Find each parasitized red blood cell.
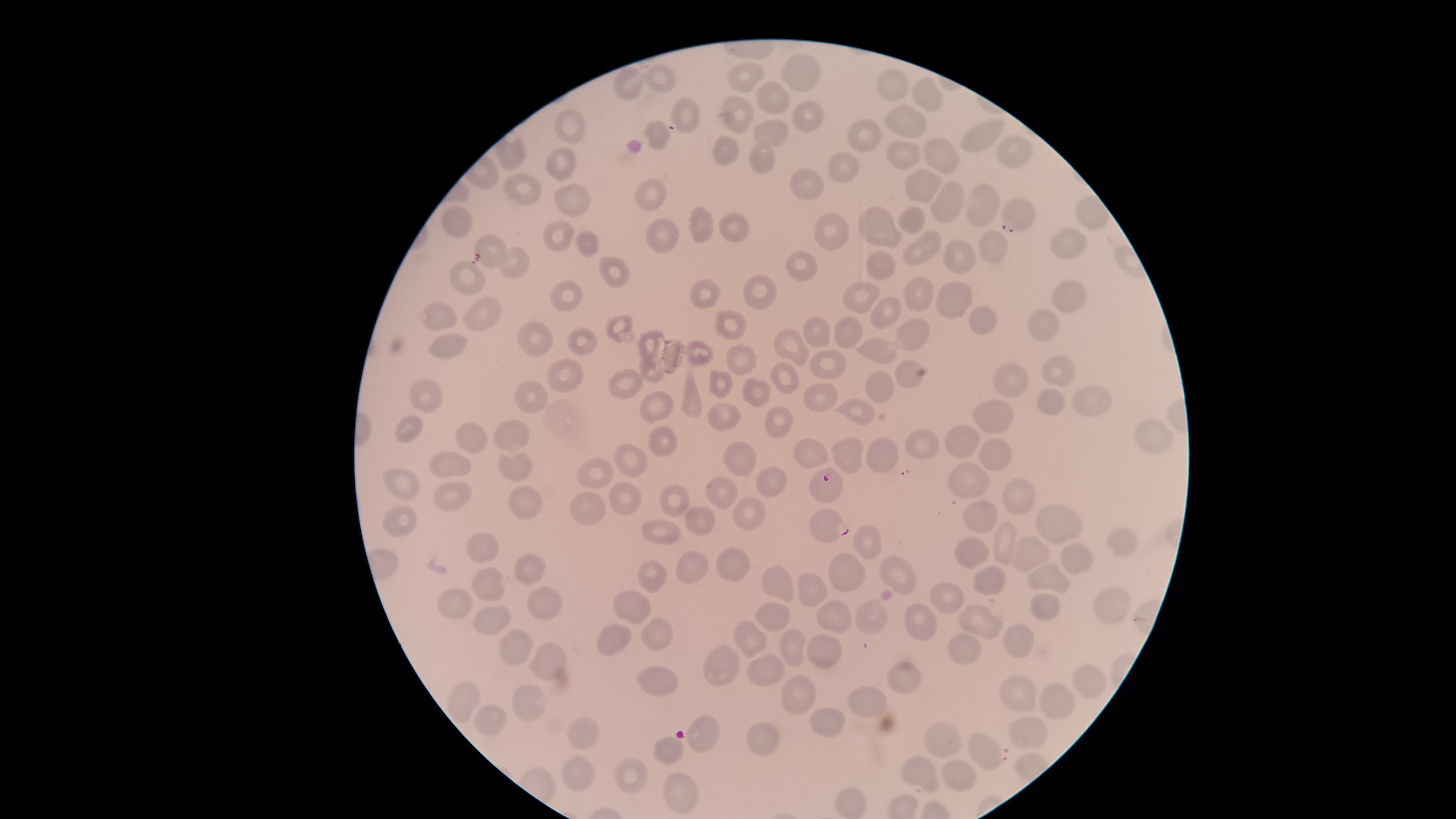
Approximate bounding boxes as [left, top, right, bottom] in pixels.
Parasitized red blood cells: [668, 97, 700, 132], [1000, 198, 1038, 234], [809, 467, 843, 504], [809, 508, 851, 543], [967, 731, 1003, 769].

uninfected red blood cells = approximate bounding boxes as [left, top, right, bottom] in pixels: [779, 54, 821, 92], [729, 61, 767, 92], [644, 65, 676, 93], [614, 68, 646, 99], [877, 69, 910, 100], [912, 77, 945, 112], [755, 80, 790, 115], [722, 96, 755, 134], [793, 100, 825, 132], [883, 103, 926, 138], [556, 109, 587, 144], [961, 118, 1006, 153], [848, 119, 882, 153], [644, 120, 670, 150], [753, 120, 789, 148], [996, 134, 1033, 168], [712, 136, 740, 166], [924, 136, 961, 174], [887, 139, 922, 169], [544, 145, 575, 181], [750, 145, 777, 173], [828, 153, 859, 182], [788, 167, 826, 200], [906, 169, 942, 203], [502, 173, 542, 206], [635, 179, 667, 212], [930, 181, 964, 222], [553, 183, 590, 217], [964, 184, 1000, 225], [441, 206, 473, 238], [687, 206, 714, 242], [858, 206, 902, 247], [898, 206, 925, 234], [814, 211, 850, 251], [718, 212, 749, 242], [645, 218, 680, 253], [543, 220, 573, 252], [1051, 228, 1088, 259], [903, 230, 940, 265], [977, 230, 1008, 262], [577, 232, 598, 257], [471, 235, 510, 268], [943, 240, 975, 274], [497, 246, 530, 279], [784, 250, 819, 281], [865, 250, 895, 281], [600, 257, 630, 287], [451, 260, 486, 295], [742, 273, 778, 311], [904, 275, 935, 311], [690, 278, 722, 310], [550, 280, 583, 311], [840, 281, 881, 312], [936, 281, 975, 318], [1052, 281, 1085, 314], [463, 296, 502, 330], [870, 296, 902, 329], [419, 301, 457, 329], [969, 305, 999, 336], [1027, 309, 1060, 341], [714, 310, 748, 340], [604, 314, 634, 343], [834, 315, 863, 348], [803, 316, 830, 346], [893, 317, 931, 350], [518, 320, 554, 357], [565, 326, 600, 356], [638, 329, 666, 360], [775, 329, 810, 367], [427, 333, 468, 359], [856, 337, 897, 365], [686, 340, 714, 366], [724, 343, 757, 376], [810, 349, 847, 379], [1040, 355, 1075, 386], [546, 358, 584, 391], [895, 358, 926, 388], [639, 359, 664, 384], [992, 361, 1029, 398], [770, 362, 799, 394], [682, 368, 703, 419], [608, 369, 642, 400], [710, 369, 734, 399], [864, 371, 895, 403], [409, 377, 443, 413], [742, 377, 772, 408], [514, 381, 549, 415], [803, 381, 838, 413], [1072, 386, 1112, 416], [1036, 388, 1065, 415], [640, 391, 673, 423], [832, 399, 877, 424], [972, 400, 1013, 433], [708, 402, 740, 430], [763, 406, 796, 438], [395, 415, 424, 445], [493, 419, 530, 451], [1134, 419, 1175, 453], [455, 421, 488, 453], [945, 425, 981, 458], [646, 426, 677, 456], [905, 429, 940, 460], [832, 435, 863, 473], [865, 437, 898, 472], [979, 438, 1013, 470], [793, 439, 829, 469], [725, 441, 758, 477], [615, 444, 648, 476], [429, 451, 472, 477], [500, 453, 534, 482], [577, 459, 614, 488], [947, 463, 991, 497], [755, 466, 788, 498], [382, 468, 422, 499], [705, 476, 738, 509], [1002, 479, 1035, 515], [434, 481, 471, 510], [608, 482, 642, 516], [506, 485, 543, 519], [660, 485, 689, 516], [569, 491, 605, 524], [733, 496, 768, 530], [961, 500, 999, 531], [1033, 503, 1081, 546], [383, 506, 417, 536], [686, 506, 716, 536], [640, 518, 680, 544], [993, 520, 1019, 565], [854, 525, 882, 560], [1108, 528, 1137, 557], [466, 531, 501, 563], [1010, 534, 1050, 573], [955, 536, 990, 569], [1060, 544, 1094, 575], [716, 547, 752, 581], [676, 550, 710, 583], [828, 552, 864, 592], [514, 553, 546, 586], [879, 554, 917, 595], [639, 561, 667, 593], [1026, 562, 1070, 592], [761, 565, 794, 602], [972, 565, 1005, 595], [472, 568, 504, 601], [798, 573, 829, 607], [929, 583, 963, 615], [1094, 586, 1130, 625], [527, 587, 563, 619], [437, 588, 472, 621], [613, 589, 652, 624], [1030, 593, 1060, 620], [815, 598, 849, 632], [856, 600, 889, 636], [753, 602, 791, 630], [904, 602, 939, 640], [958, 604, 1004, 640], [471, 606, 510, 637], [640, 618, 672, 649], [733, 620, 767, 658], [596, 623, 632, 656], [1003, 623, 1035, 658], [499, 628, 532, 665], [779, 628, 807, 666], [806, 632, 843, 669], [947, 633, 981, 664], [529, 641, 566, 681], [703, 644, 740, 686], [747, 654, 784, 685], [886, 662, 920, 694], [1075, 664, 1108, 700], [636, 666, 678, 696], [781, 674, 817, 714], [999, 675, 1036, 711], [447, 681, 480, 723], [513, 683, 549, 721], [1039, 684, 1076, 718], [847, 686, 887, 719], [474, 703, 508, 735], [811, 707, 846, 737], [686, 715, 720, 753], [568, 716, 598, 750], [1009, 717, 1049, 748], [746, 721, 780, 756], [926, 722, 962, 759], [653, 736, 683, 765], [563, 755, 593, 789], [903, 755, 940, 792], [613, 758, 648, 793], [942, 760, 975, 790], [665, 771, 697, 812], [835, 786, 866, 818]
species = Plasmodium falciparum
visible region = circular
stain = Giemsa
preparation = thin blood film
capture = smartphone photograph through the microscope eyepiece
image size = 1456×819 pixels
field of view = single